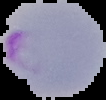
Summary:
  - Image size: 106×100 pixels
  - Preparation: thin blood smear
  - Result: Plasmodium parasites identified
  - Image type: segmented cell region with the area outside set to black